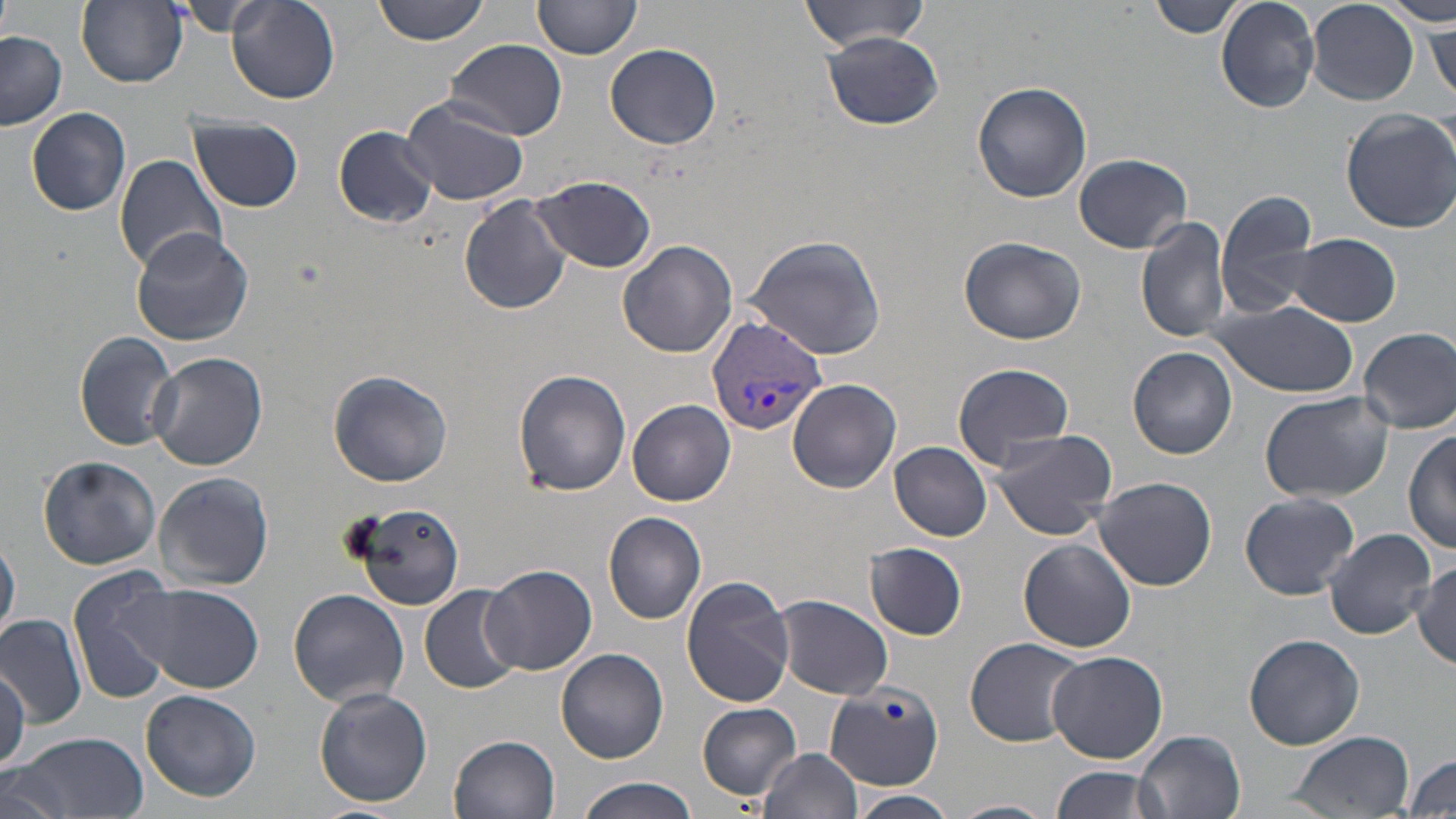

{
  "slide_level_diagnosis": "Plasmodium vivax",
  "magnification": "1000x",
  "uninfected_red_blood_cell_locations": "approximate bounding boxes as [x1, y1, x2, y2] in pixels: [375, 0, 489, 44], [533, 0, 643, 60], [801, 0, 931, 52], [1149, 0, 1245, 39], [1216, 0, 1320, 114], [1388, 0, 1455, 26], [77, 1, 187, 88], [1307, 1, 1419, 105], [228, 2, 340, 104], [181, 3, 258, 37], [1428, 19, 1455, 104], [0, 31, 66, 130], [820, 31, 944, 130], [445, 38, 566, 141], [605, 42, 722, 149], [972, 81, 1093, 203], [400, 93, 533, 206], [25, 107, 133, 216], [1340, 108, 1456, 233], [193, 116, 304, 211], [333, 126, 438, 228], [1073, 152, 1193, 253], [113, 154, 229, 274], [529, 175, 658, 273], [1215, 189, 1319, 320], [459, 194, 573, 314], [1136, 216, 1231, 344], [131, 229, 256, 346], [1289, 233, 1403, 327], [744, 234, 888, 358], [958, 236, 1086, 345], [618, 240, 737, 358], [1209, 299, 1356, 397], [1359, 327, 1456, 434], [74, 331, 178, 451], [1128, 347, 1239, 459], [150, 353, 268, 472], [951, 360, 1076, 468], [328, 369, 453, 487], [513, 369, 631, 496], [788, 379, 902, 493], [1259, 391, 1393, 501], [629, 399, 736, 506], [988, 426, 1119, 541], [1405, 427, 1456, 555], [890, 442, 992, 540], [37, 455, 162, 570], [153, 472, 275, 592], [1093, 475, 1217, 590], [1241, 492, 1360, 598], [352, 500, 465, 609], [603, 511, 707, 623], [1325, 528, 1434, 639], [1, 534, 20, 647], [1019, 537, 1136, 652], [865, 542, 967, 640], [1411, 560, 1456, 668], [480, 565, 596, 676], [69, 566, 183, 704], [680, 574, 798, 708], [141, 585, 263, 694], [419, 585, 523, 694], [288, 588, 410, 707], [775, 594, 894, 699], [1, 614, 89, 728], [1244, 633, 1365, 750], [965, 636, 1085, 746], [556, 648, 669, 763], [1045, 649, 1167, 764], [0, 663, 28, 770], [824, 678, 943, 789], [313, 687, 435, 808], [141, 689, 261, 802], [698, 703, 801, 798], [1135, 729, 1246, 819], [1285, 730, 1413, 816], [8, 731, 148, 819], [450, 733, 562, 819], [759, 746, 863, 819], [1405, 752, 1456, 818], [1049, 764, 1160, 819], [1, 770, 74, 819], [577, 776, 699, 819], [852, 790, 958, 818], [949, 799, 1057, 818]",
  "plasmodium_vivax_infected_red_blood_cell_locations": "approximate bounding boxes as [x1, y1, x2, y2] in pixels: [706, 314, 829, 435]",
  "modality": "optical microscopy",
  "preparation": "thin blood smear",
  "field_of_view": "single",
  "stain": "May-Grünwald-Giemsa",
  "image_size": "1456×819 pixels"
}